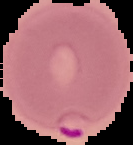

image size = 133×145 pixels
image type = segmented cell region with the area outside set to black
result = Plasmodium parasites identified
preparation = thin blood smear